Assess this cell for malaria.
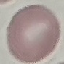
It is uninfected.

Giemsa-stained preparation. Thin blood smear. Automatically extracted cell patch, resized to 64 × 64 pixels. Photographed with a smartphone camera at the microscope eyepiece.